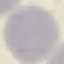

Summary:
  - Malaria status: uninfected
  - Stain: Giemsa
  - Capture: smartphone through the microscope eyepiece
  - Image type: automatically extracted cell patch, resized to 64 × 64 pixels
  - Preparation: thin smear